Locate every malaria parasite and every leukocyte.
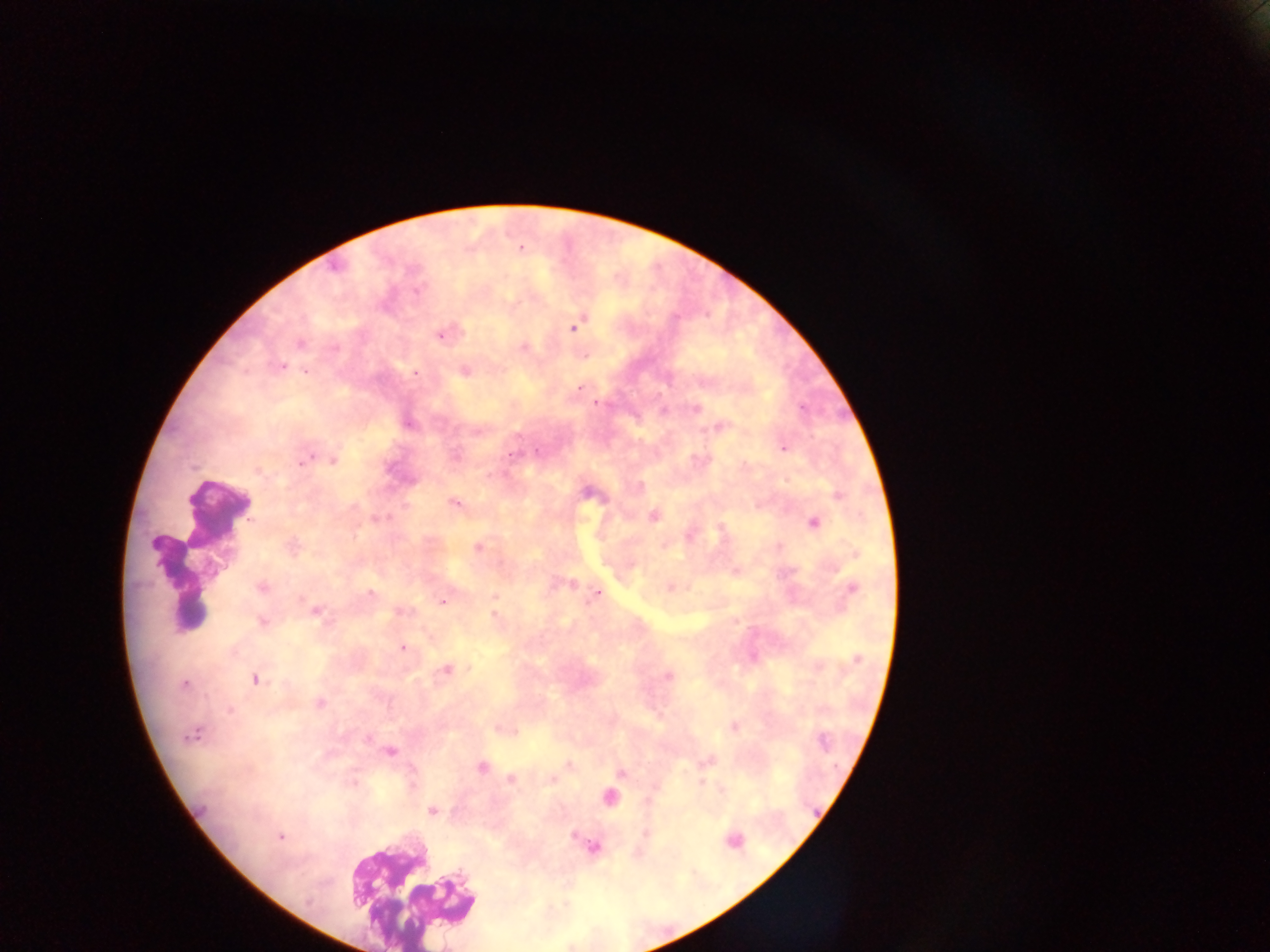
Approximate centers as (x, y) in pixels.
Malaria parasites: (520, 248), (574, 326), (440, 333), (299, 343), (523, 347), (280, 366), (464, 369), (305, 370), (579, 387), (595, 402), (695, 407), (407, 423), (719, 426), (783, 447), (304, 457), (332, 459), (257, 470), (454, 503), (652, 516), (377, 519), (814, 522), (292, 546), (478, 547), (854, 553), (735, 570), (261, 587), (670, 587), (852, 589), (597, 592), (370, 594), (495, 596), (443, 600), (314, 610), (400, 612), (494, 615), (263, 622), (401, 647), (856, 660), (445, 669), (667, 676), (255, 679), (185, 684), (319, 703), (733, 727), (501, 729), (191, 734), (389, 751), (707, 760), (568, 765), (480, 766), (620, 772), (510, 778), (551, 779), (702, 783), (432, 811), (279, 836), (593, 847).
Leukocytes: (216, 509), (181, 578), (731, 841), (411, 887), (446, 899).
One object is labeled both malaria parasite and leukocyte by the source: (609, 797).

Photographed through a microscope with a mobile-phone camera. Image is 1270×952 pixels. Thick blood film. Sample from Ghana. Single field of view.